Identify the blood parasite species.
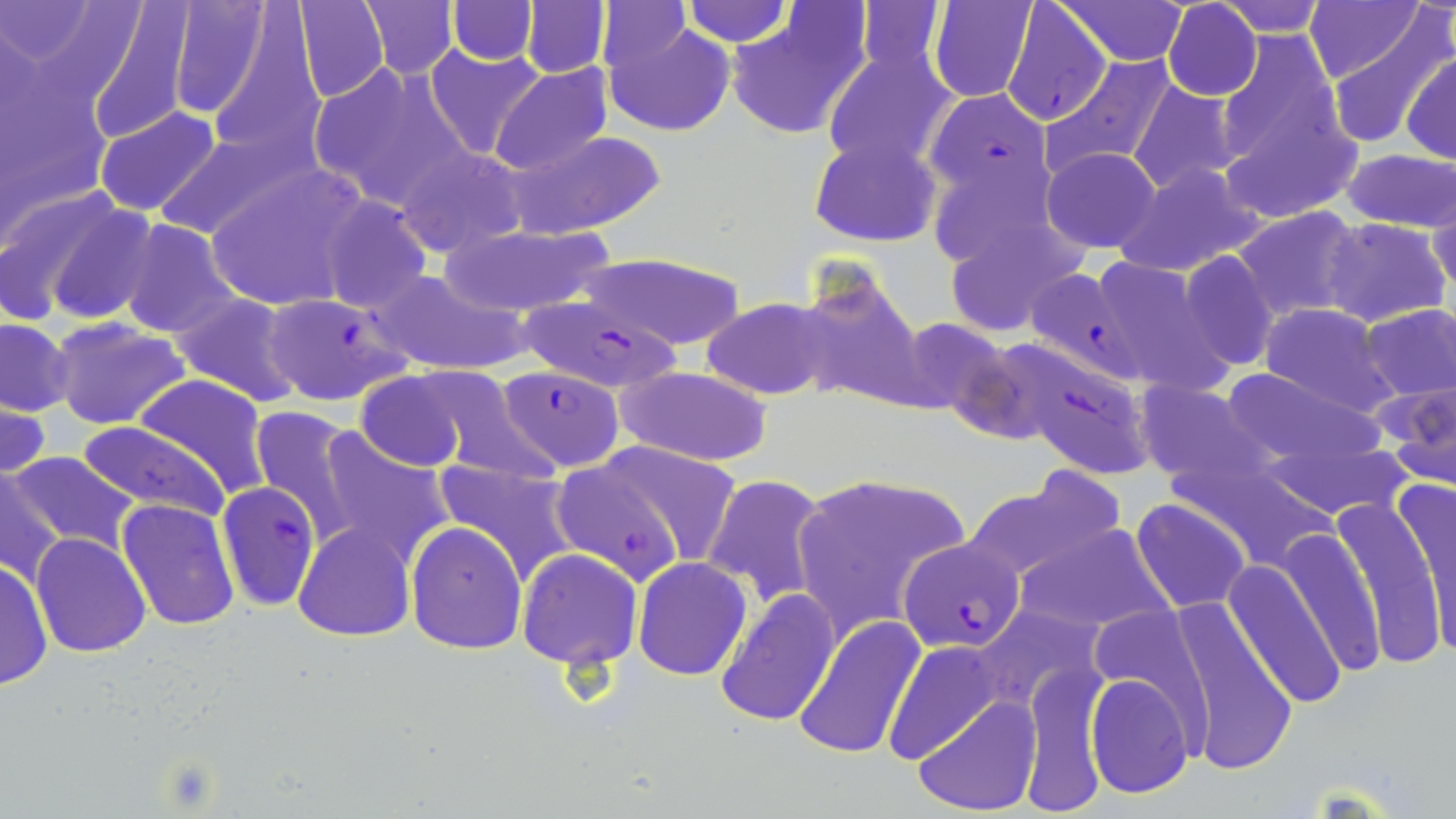

Plasmodium falciparum.

uninfected_red_blood_cell_locations: 'approximate bounding boxes as [x1, y1, x2, y2] in pixels: [166, 0, 277, 123], [289, 0, 390, 103], [358, 0, 459, 80], [446, 0, 539, 64], [522, 0, 610, 78], [679, 0, 794, 48], [850, 0, 952, 84], [1306, 0, 1423, 84], [1, 1, 98, 64], [83, 1, 198, 145], [1061, 1, 1187, 64], [1162, 1, 1262, 101], [1216, 1, 1332, 36], [595, 2, 690, 75], [926, 2, 1041, 104], [726, 5, 870, 142], [215, 7, 348, 143], [1320, 9, 1452, 147], [603, 16, 735, 138], [1216, 31, 1353, 190], [424, 45, 547, 161], [821, 46, 958, 175], [0, 48, 111, 236], [1402, 51, 1456, 164], [1038, 54, 1179, 180], [307, 60, 468, 208], [491, 63, 615, 177], [1128, 81, 1241, 195], [94, 107, 221, 218], [147, 127, 312, 243], [505, 130, 667, 239], [809, 133, 943, 248], [396, 145, 527, 258], [1040, 146, 1163, 253], [1342, 148, 1456, 233], [1112, 161, 1268, 277], [204, 165, 367, 313], [1429, 187, 1456, 298], [11, 189, 158, 328], [317, 194, 434, 314], [1232, 206, 1365, 322], [940, 216, 1086, 340], [1323, 217, 1451, 328], [116, 219, 243, 341], [438, 223, 618, 316], [1176, 251, 1279, 371], [582, 252, 746, 348], [1085, 254, 1233, 391], [370, 267, 534, 377], [790, 269, 928, 411], [169, 292, 307, 407], [701, 296, 840, 402], [1258, 303, 1400, 416], [1359, 303, 1456, 402], [1, 317, 75, 416], [892, 317, 1014, 419], [49, 319, 191, 431], [405, 366, 553, 482], [614, 366, 775, 466], [1219, 367, 1379, 464], [355, 369, 473, 474], [133, 374, 274, 499], [1372, 374, 1456, 489], [1136, 380, 1269, 487], [0, 394, 51, 485], [248, 406, 365, 547], [77, 420, 230, 526], [307, 427, 454, 568], [1259, 427, 1414, 521], [611, 448, 740, 565], [7, 449, 141, 557], [432, 457, 582, 584], [1, 468, 66, 589], [701, 472, 830, 609], [963, 475, 1122, 582], [1391, 475, 1456, 659], [819, 481, 984, 584], [1331, 492, 1447, 669], [117, 498, 238, 632], [1131, 498, 1251, 613], [795, 515, 902, 640], [406, 520, 528, 654], [293, 523, 416, 641], [1014, 523, 1171, 635], [1279, 526, 1382, 676], [31, 532, 153, 657], [515, 547, 643, 669], [0, 556, 52, 692], [632, 556, 753, 680], [1224, 559, 1345, 710], [713, 586, 839, 727], [973, 602, 1108, 714], [1172, 605, 1298, 776], [797, 617, 926, 761], [885, 638, 1001, 764], [1020, 664, 1109, 816], [1085, 671, 1195, 800], [913, 695, 1039, 814]'
plasmodium_falciparum_infected_red_blood_cell_locations: 'approximate bounding boxes as [x1, y1, x2, y2] in pixels: [1000, 2, 1112, 127], [924, 87, 1052, 211], [1030, 271, 1153, 392], [262, 291, 413, 406], [519, 297, 689, 385], [1000, 340, 1158, 482], [497, 366, 625, 470], [555, 461, 685, 581], [217, 482, 321, 612], [899, 536, 1027, 653]'
stain: May-Grünwald-Giemsa
field_of_view: one of a larger specimen
preparation: thin blood smear
image_size: 1456×819 pixels
magnification: 1000x
modality: optical microscopy